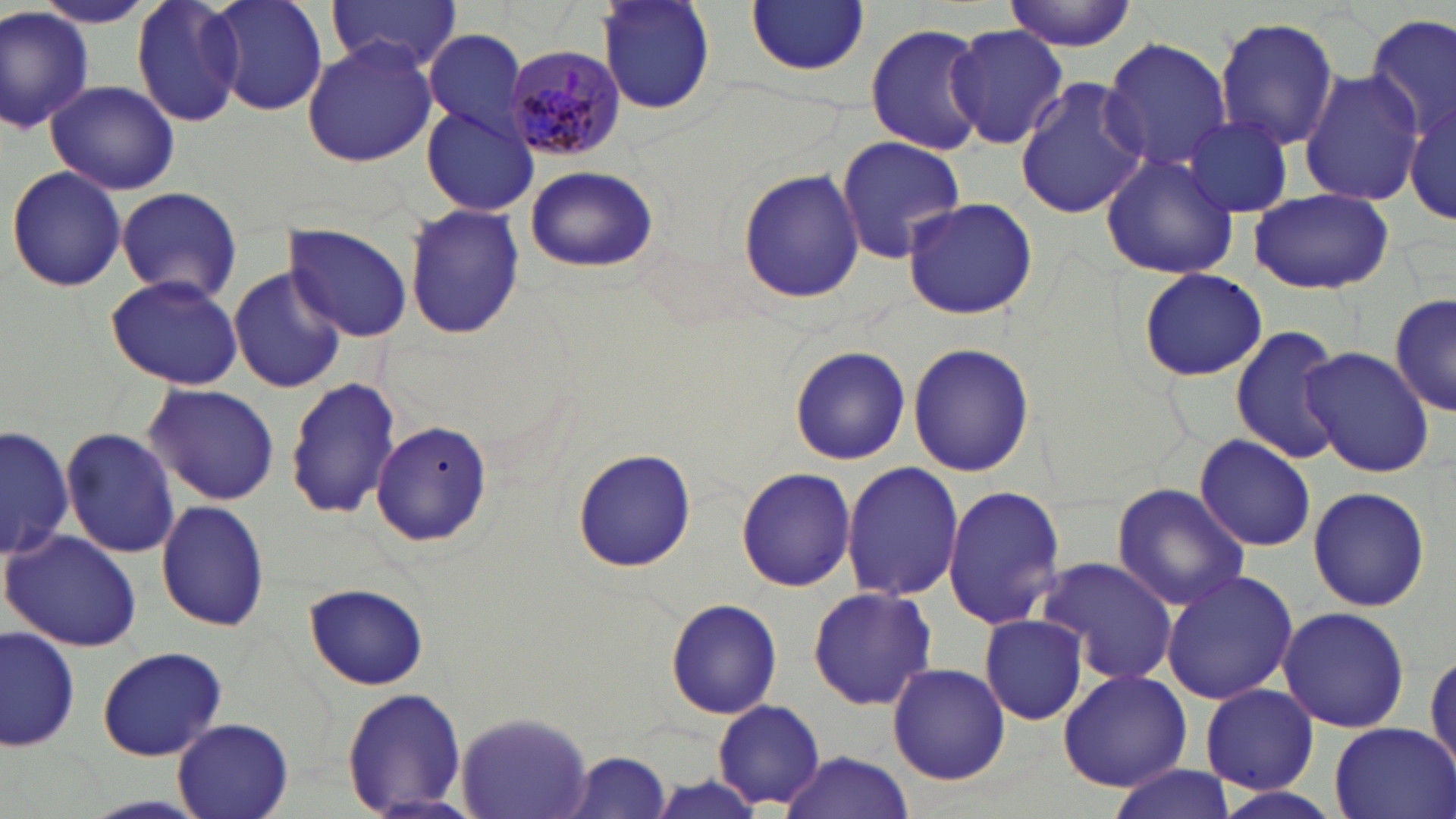
Approximate bounding boxes as (x1,y1)-(x2,y2) corner pairs in pixels. Plasmodium malariae-infected red blood cell locations: (504,39)-(623,164). Uninfected red blood cell locations: (131,0)-(244,124), (209,0)-(332,115), (326,0)-(463,72), (595,0)-(716,118), (1003,1)-(1137,51), (27,2)-(162,31), (746,2)-(870,76), (0,5)-(96,136), (1363,14)-(1454,148), (1214,16)-(1341,150), (864,22)-(989,155), (945,24)-(1068,150), (421,29)-(533,141), (1100,37)-(1234,173), (301,38)-(439,168), (1299,70)-(1424,207), (1014,77)-(1148,221), (47,80)-(180,195), (1407,95)-(1455,225), (420,105)-(539,217), (1181,116)-(1296,218), (836,135)-(966,263), (1101,153)-(1239,280), (524,165)-(657,274), (6,166)-(125,291), (737,167)-(864,304), (115,185)-(242,303), (1246,186)-(1393,294), (900,197)-(1038,320), (402,203)-(526,339), (284,223)-(412,341), (227,267)-(345,394), (1138,268)-(1267,382), (104,272)-(244,389), (1389,288)-(1456,419), (1229,325)-(1347,466), (907,343)-(1033,476), (786,345)-(912,465), (1301,346)-(1433,477), (286,375)-(402,520), (141,383)-(282,505), (369,421)-(493,548), (1,423)-(73,566), (60,426)-(181,559), (1193,433)-(1317,551), (571,448)-(697,574), (842,459)-(963,603), (736,465)-(855,592), (1112,482)-(1250,612), (942,485)-(1066,630), (1307,485)-(1431,613), (156,499)-(269,632), (0,530)-(142,650), (1037,556)-(1179,684), (1161,568)-(1301,703), (303,581)-(430,692), (807,586)-(936,711), (663,597)-(784,720), (1275,607)-(1412,733), (979,614)-(1089,726), (1,625)-(80,753), (96,644)-(228,760), (1425,647)-(1456,775), (889,663)-(1009,785), (1057,668)-(1190,791), (1201,684)-(1319,794), (340,686)-(468,817), (711,699)-(826,810), (456,711)-(593,818), (171,717)-(294,819), (1326,721)-(1456,819), (778,750)-(915,819), (562,751)-(673,818), (1108,765)-(1234,819), (1208,783)-(1343,819). Slide-level diagnosis: Plasmodium malariae. May-Grünwald-Giemsa stain. Image is 1456×819 pixels. One field of a larger specimen. Thin blood smear. Captured at 1000x magnification. Light microscopy.